Locate platelets.
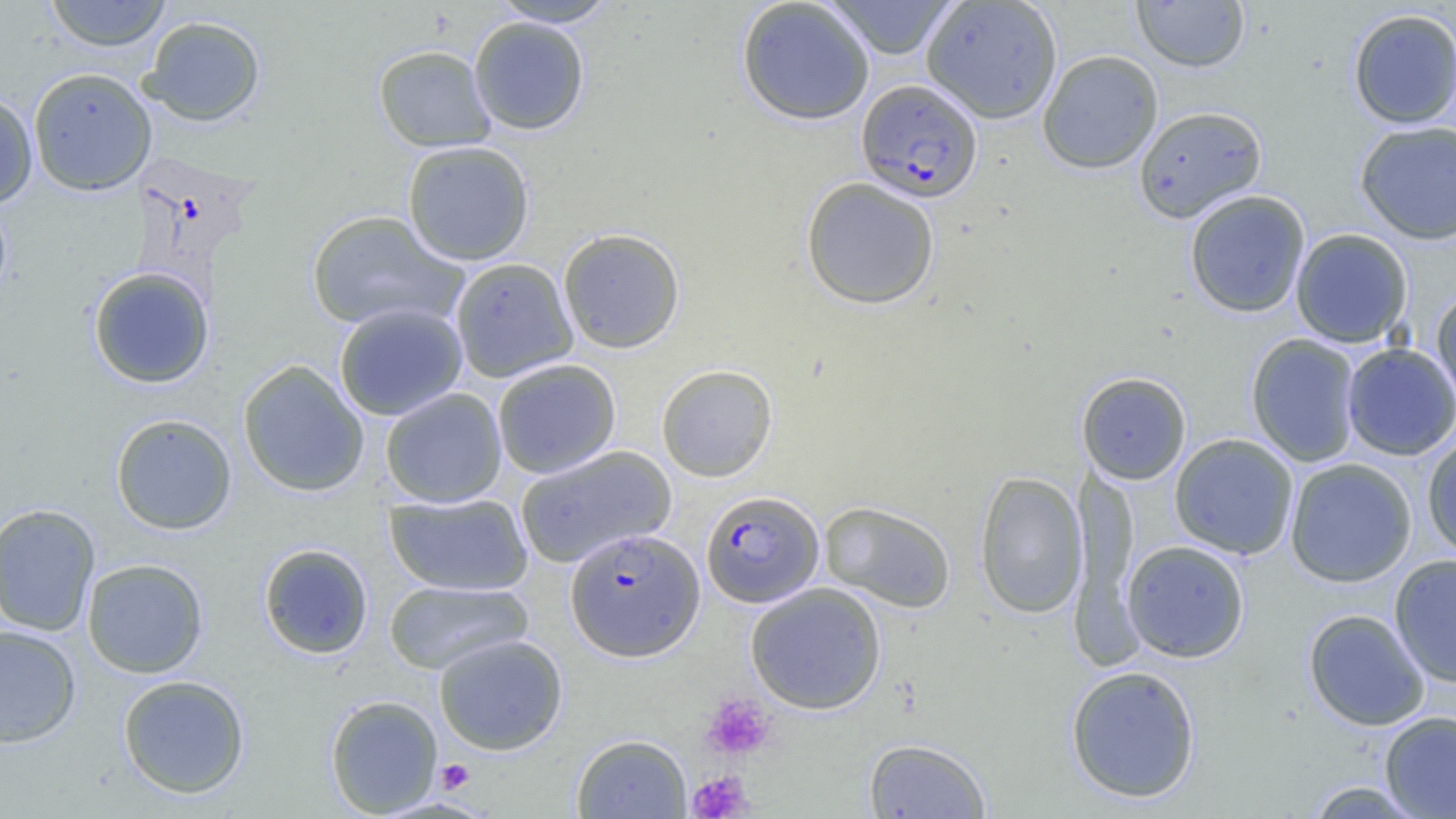
Approximate bounding boxes as (x1, y1, x2, y2) in pixels.
Platelets: (700, 692, 778, 761), (436, 759, 474, 794), (687, 769, 754, 818).

slide-level diagnosis = Plasmodium falciparum
field of view = one of a larger specimen
preparation = thin blood film
Plasmodium falciparum-infected red blood cell locations = approximate bounding boxes as (x1, y1, x2, y2) in pixels: (856, 78, 984, 204), (701, 489, 824, 608), (565, 528, 705, 661)
uninfected red blood cell locations = approximate bounding boxes as (x1, y1, x2, y2) in pixels: (44, 0, 172, 52), (736, 0, 875, 126), (822, 0, 960, 59), (1131, 0, 1250, 73), (488, 1, 622, 28), (920, 1, 1064, 124), (1347, 8, 1456, 129), (141, 15, 266, 127), (468, 16, 591, 135), (373, 44, 497, 152), (1037, 49, 1164, 174), (28, 67, 158, 196), (0, 91, 38, 208), (1133, 105, 1267, 223), (1355, 120, 1456, 245), (402, 140, 535, 266), (801, 176, 940, 310), (1184, 190, 1311, 318), (0, 195, 13, 307), (307, 210, 466, 332), (558, 227, 685, 354), (1290, 228, 1413, 348), (450, 257, 578, 382), (87, 265, 215, 389), (1431, 285, 1456, 412), (334, 303, 468, 421), (1245, 333, 1362, 467), (1341, 342, 1456, 461), (491, 359, 622, 479), (238, 360, 370, 497), (656, 364, 778, 482), (1076, 371, 1192, 484), (380, 388, 507, 507), (110, 413, 238, 535), (1421, 430, 1456, 561), (1169, 433, 1299, 560), (514, 445, 677, 569), (1284, 458, 1418, 587), (1069, 460, 1141, 652), (973, 471, 1088, 619), (384, 491, 534, 596), (819, 500, 957, 614), (0, 502, 101, 637), (1121, 540, 1250, 663), (258, 543, 374, 659), (1389, 554, 1456, 688), (82, 558, 209, 678), (384, 580, 532, 675), (744, 582, 887, 715), (1303, 608, 1431, 731), (0, 624, 82, 748), (433, 634, 568, 755), (1064, 664, 1202, 804), (118, 674, 251, 798), (325, 694, 444, 816), (1379, 710, 1456, 818), (571, 734, 692, 818), (863, 738, 992, 818), (1303, 780, 1431, 819)
modality = light microscopy
magnification = 1000x
image size = 1456×819 pixels